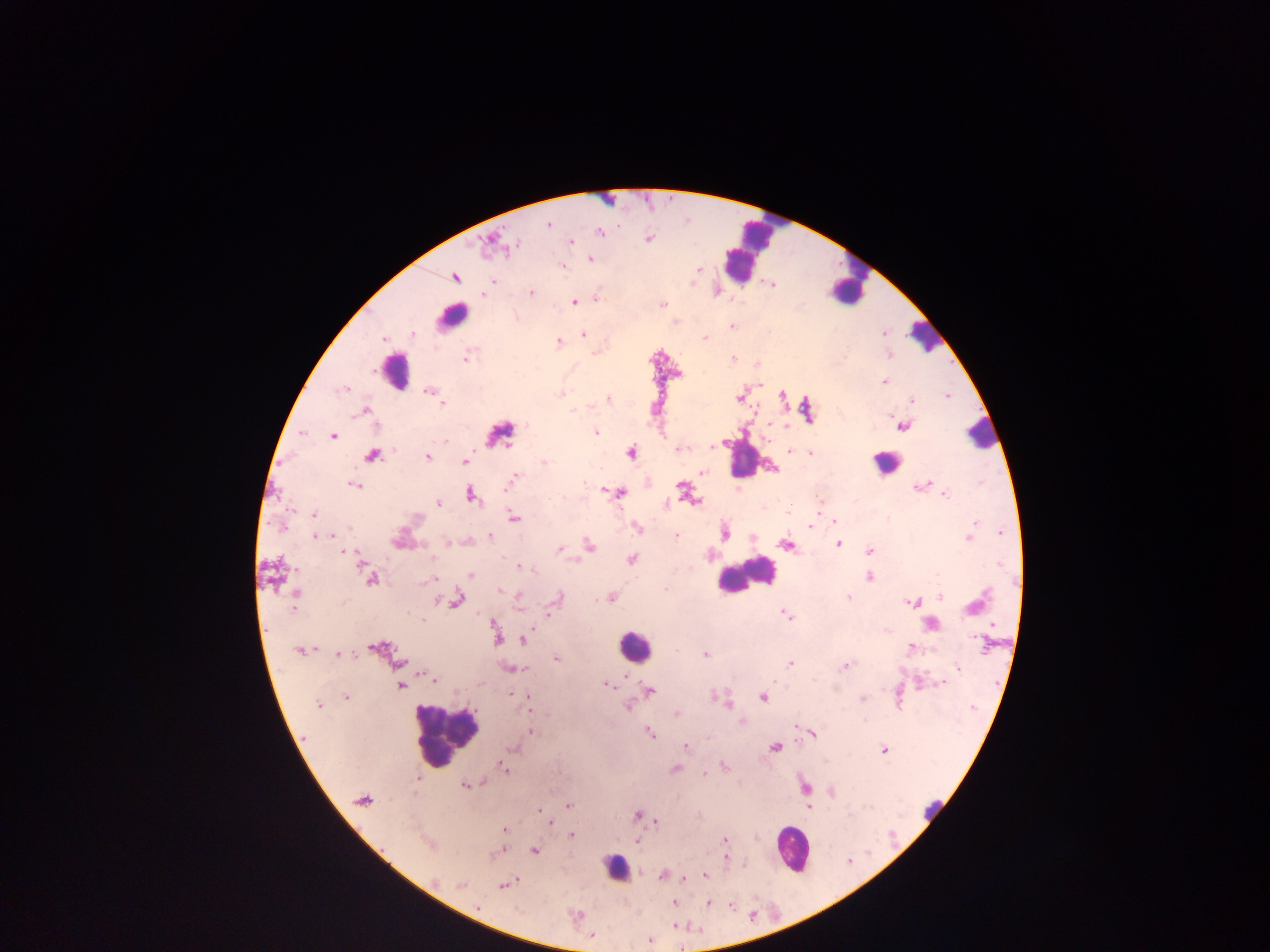
Approximate centers as (x, y) in pixels.
Summary:
  - Leukocyte locations (subset; some below the resolvable size): (769, 227), (741, 259), (860, 263), (847, 289), (451, 316), (923, 336), (395, 372), (981, 434), (742, 457), (885, 463), (743, 576), (635, 646), (446, 735), (932, 813), (792, 849), (615, 868)
  - Plasmodium parasite locations: (548, 224), (600, 232), (648, 238), (571, 241), (488, 242), (515, 245), (591, 259), (563, 266), (699, 269), (454, 277), (493, 281), (772, 285), (531, 292), (484, 295), (597, 298), (574, 302), (663, 304), (731, 326), (413, 334), (884, 334), (583, 335), (704, 338), (383, 339), (558, 342), (466, 356), (732, 359), (884, 382), (346, 389), (429, 391), (559, 394), (782, 395), (947, 396), (740, 397), (608, 399), (912, 401), (442, 404), (367, 410), (902, 426), (597, 432), (302, 434), (333, 436), (445, 442), (712, 447), (678, 449), (790, 451), (631, 452), (810, 453), (372, 456), (427, 457), (465, 461), (544, 462), (703, 473), (514, 476), (510, 482), (355, 485), (920, 486), (681, 487), (620, 494), (471, 495), (945, 495), (438, 502), (818, 509), (313, 514), (514, 517), (835, 521), (974, 523), (282, 528), (636, 528), (810, 528), (971, 532), (1001, 533), (724, 534), (332, 535), (490, 535), (314, 536), (676, 536), (969, 537), (448, 542), (786, 544), (838, 544), (589, 545), (559, 548), (345, 551), (870, 551), (359, 559), (632, 559), (362, 567), (521, 567), (471, 575), (870, 577), (370, 579), (432, 579), (499, 590), (295, 593), (940, 596), (519, 597), (612, 597), (558, 598), (849, 598), (457, 601), (912, 602), (972, 606), (294, 607), (549, 614), (787, 614), (421, 619), (992, 626), (496, 636), (975, 638), (523, 640), (911, 646), (376, 647), (298, 650), (339, 654), (704, 654), (556, 658), (790, 664), (845, 666), (510, 668), (958, 668), (523, 670), (433, 680), (942, 682), (607, 684), (919, 684), (400, 686), (649, 691), (525, 696), (346, 698), (762, 698), (861, 698), (528, 703), (727, 703), (318, 705), (628, 706), (676, 714), (741, 722), (532, 732), (650, 733), (813, 734), (686, 747), (775, 748), (514, 749), (884, 749), (724, 766), (504, 768), (675, 769), (704, 774), (417, 779), (481, 783), (465, 785), (805, 787), (363, 799), (568, 806), (809, 808), (541, 811), (638, 815), (656, 821), (550, 822), (503, 829), (571, 834), (724, 841), (533, 850), (498, 852), (725, 857), (663, 875), (705, 875), (435, 881), (461, 884), (503, 886), (674, 903), (708, 903), (477, 907), (574, 915), (592, 935), (649, 940)
  - Field of view: single
  - Preparation: thick blood film
  - Capture: mobile-phone photograph through a microscope
  - Image size: 1270×952 pixels
  - Country: Ghana